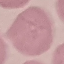
malaria status = uninfected
image type = cell patch, automatically extracted from a larger field of view and resized to 64 × 64 pixels
stain = Giemsa
preparation = thin smear
capture = smartphone camera at the microscope eyepiece